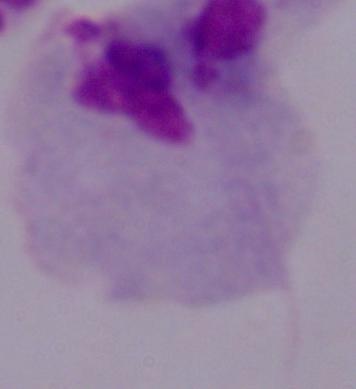

modality = micrograph
magnification = 1000x
identification = trichomonad